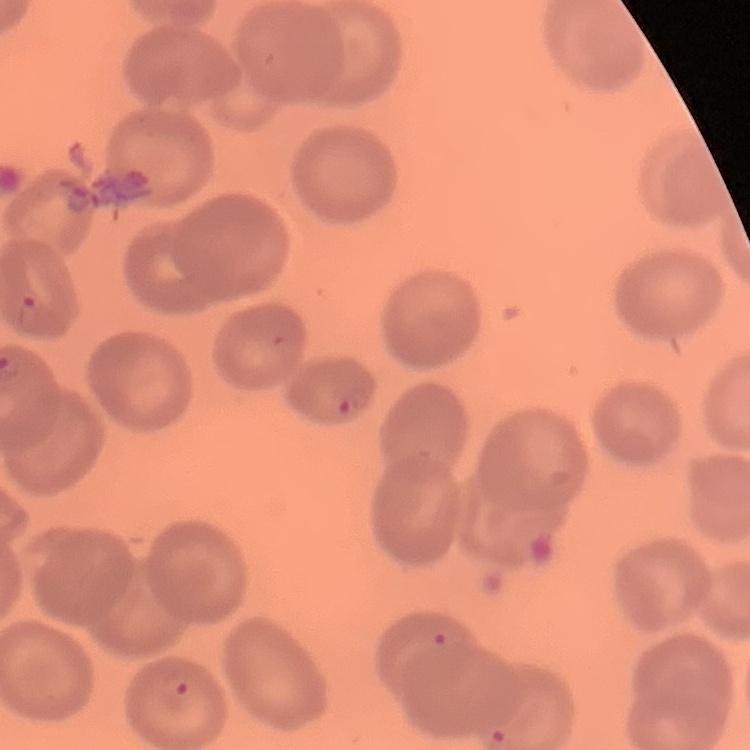
Summary:
  - Erythrocyte morphology: no rouleaux formation
  - Image type: one tile cut from a larger photomicrograph
  - Stain: Field's or Giemsa
  - Preparation: thin blood film